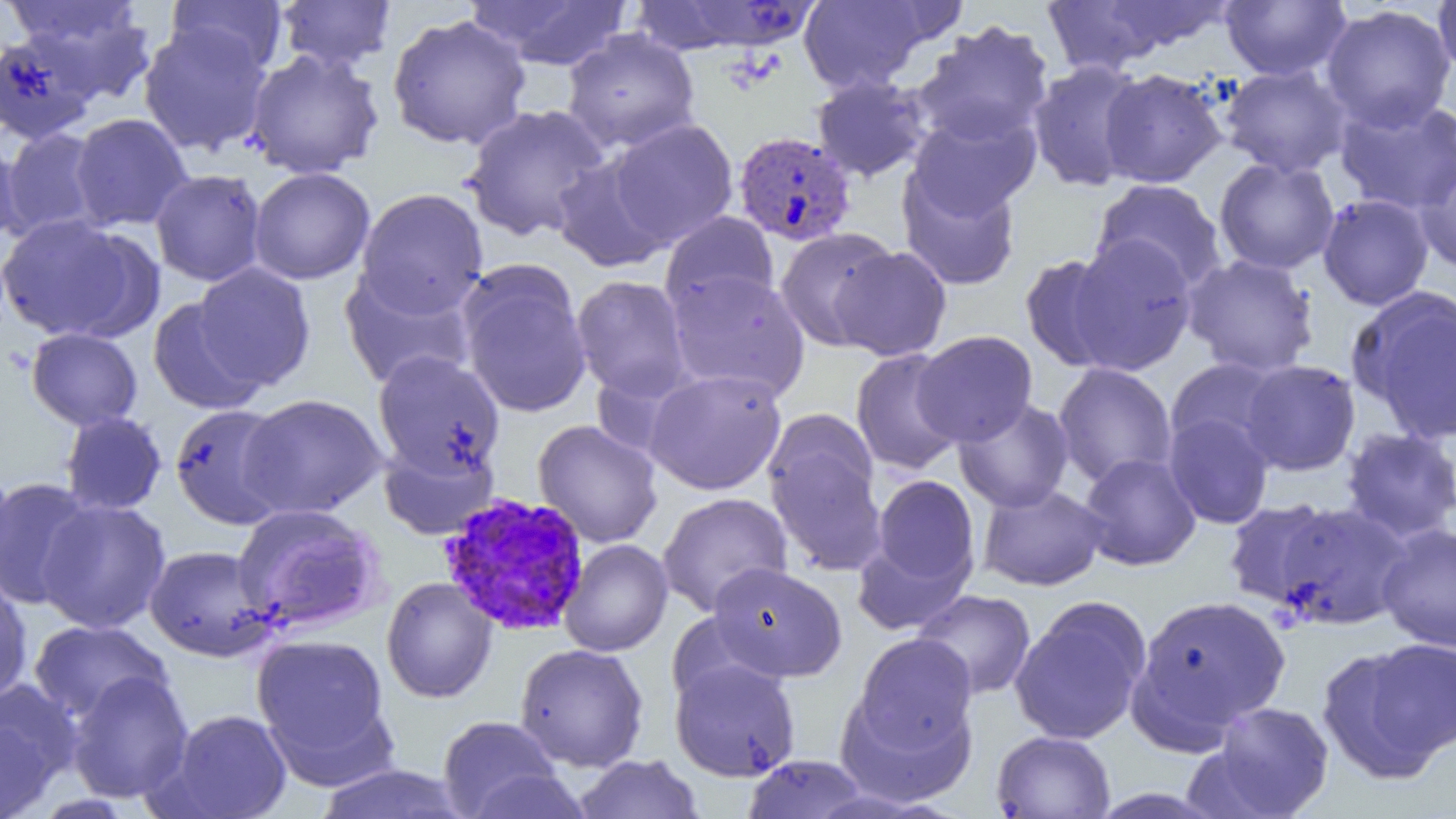
Approximate bounding boxes as (x1, y1, x2, y2) in pixels. Plasmodium vivax-infected red blood cell locations: (733, 131, 857, 247), (438, 492, 592, 636). Uninfected red blood cell locations: (465, 0, 635, 71), (798, 0, 941, 94), (1220, 0, 1352, 81), (1433, 0, 1456, 82), (166, 1, 288, 77), (274, 1, 398, 72), (632, 1, 815, 55), (1038, 1, 1180, 77), (1093, 1, 1235, 53), (8, 2, 156, 104), (1320, 5, 1456, 132), (387, 14, 532, 150), (912, 20, 1054, 147), (138, 24, 273, 156), (561, 29, 701, 153), (1, 31, 101, 144), (245, 49, 384, 179), (1026, 59, 1149, 192), (1220, 64, 1352, 178), (1098, 68, 1228, 188), (811, 74, 933, 182), (1334, 95, 1456, 215), (460, 104, 612, 242), (908, 110, 1041, 219), (70, 113, 193, 231), (606, 118, 739, 248), (1, 127, 105, 240), (0, 137, 24, 249), (1413, 152, 1456, 273), (551, 153, 674, 273), (1214, 157, 1339, 275), (896, 166, 1022, 291), (249, 167, 375, 285), (150, 169, 266, 287), (1090, 179, 1227, 294), (355, 187, 489, 318), (1317, 193, 1434, 310), (659, 211, 779, 316), (0, 214, 152, 342), (774, 227, 900, 351), (1067, 236, 1198, 375), (830, 246, 953, 361), (1020, 254, 1126, 372), (1182, 254, 1320, 378), (192, 263, 316, 391), (456, 266, 593, 418), (339, 267, 477, 390), (666, 269, 811, 401), (570, 275, 693, 401), (1348, 287, 1456, 444), (148, 296, 268, 415), (26, 327, 143, 430), (913, 330, 1038, 446), (850, 348, 966, 476), (372, 350, 505, 478), (1165, 358, 1283, 457), (1239, 360, 1361, 476), (1052, 363, 1178, 488), (644, 368, 786, 496), (239, 393, 387, 519), (953, 397, 1075, 513), (169, 403, 294, 530), (59, 411, 167, 516), (1162, 411, 1274, 529), (533, 419, 663, 548), (764, 420, 886, 574), (1340, 427, 1456, 543), (379, 440, 499, 540), (1078, 452, 1201, 571), (0, 462, 16, 589), (871, 475, 980, 589), (0, 476, 99, 610), (978, 484, 1108, 591), (657, 492, 793, 616), (1222, 498, 1340, 611), (36, 499, 171, 634), (1270, 502, 1411, 630), (232, 503, 385, 634), (1376, 523, 1456, 653), (852, 536, 973, 636), (559, 539, 672, 657), (145, 545, 278, 661), (708, 562, 848, 682), (0, 576, 33, 705), (381, 576, 497, 703), (911, 589, 1036, 700), (1130, 593, 1292, 740), (1009, 596, 1152, 746), (29, 619, 171, 724), (251, 633, 392, 774), (851, 633, 978, 755), (1318, 640, 1456, 779), (513, 643, 649, 772), (670, 658, 801, 781), (66, 670, 194, 804), (0, 679, 81, 812), (835, 683, 977, 807), (1203, 701, 1335, 818), (160, 709, 293, 819), (437, 715, 566, 818), (991, 730, 1116, 819), (572, 754, 705, 818), (741, 754, 873, 818), (312, 763, 473, 819), (457, 768, 594, 818), (1085, 787, 1228, 818). Slide-level diagnosis: Plasmodium vivax. Captured at 1000x magnification. Thin blood film. Single field of view. Image is 1456×819 pixels. Light microscopy.